Identify the preparation type.
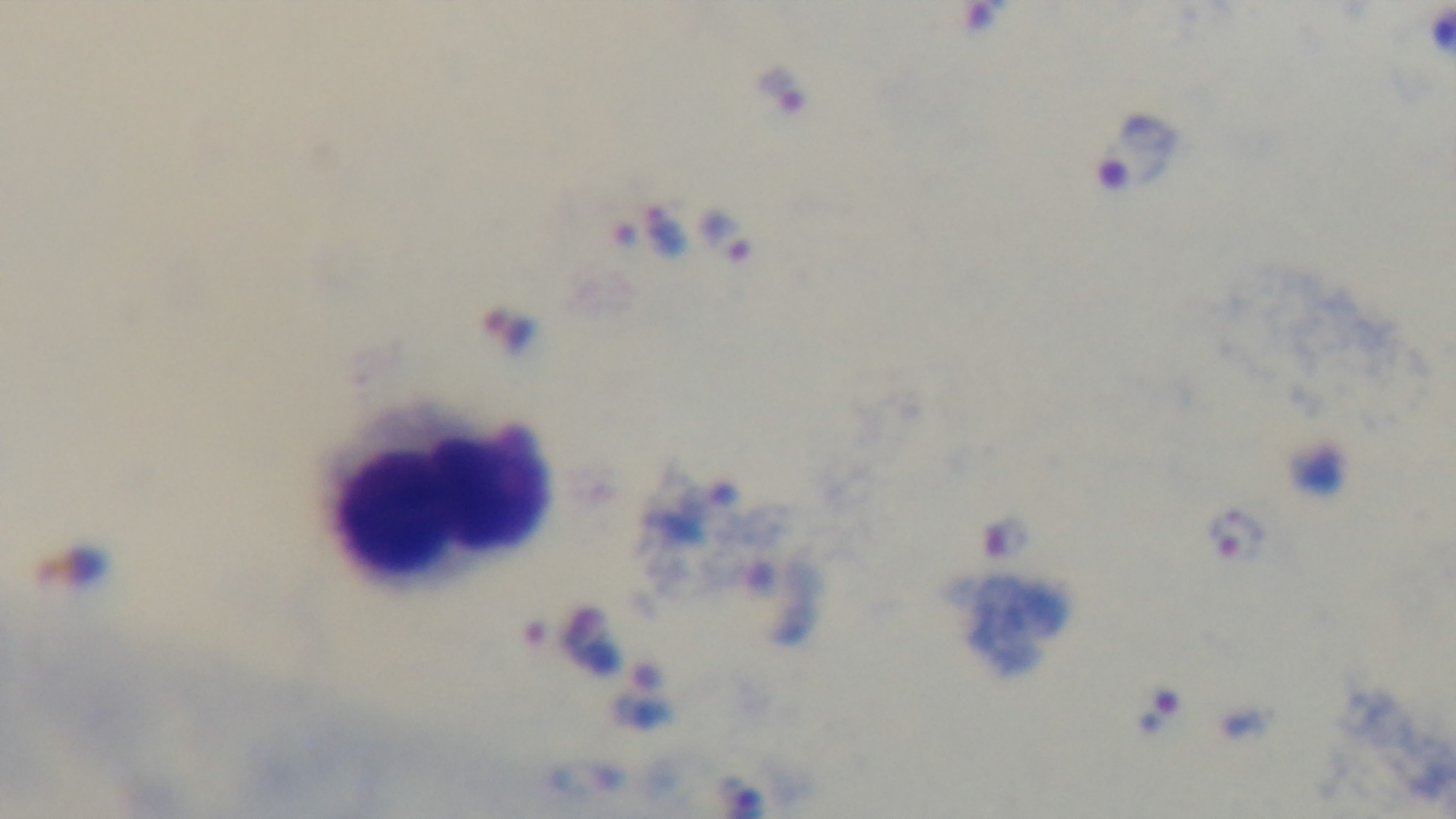
Thick.

Summary:
  - Field of view: one from the slide
  - Stain: Giemsa
  - Capture: mounted 4K digital camera
  - Modality: light microscopy
  - Malaria status: infected
  - Objective: 100x oil immersion